Name the parasite shown.
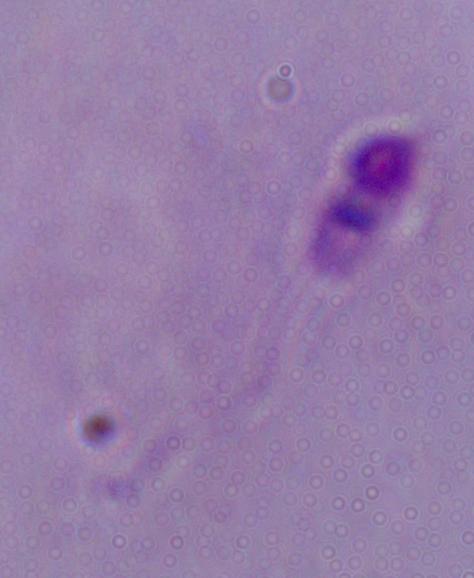

Leishmania.

1000x magnification. Micrograph.